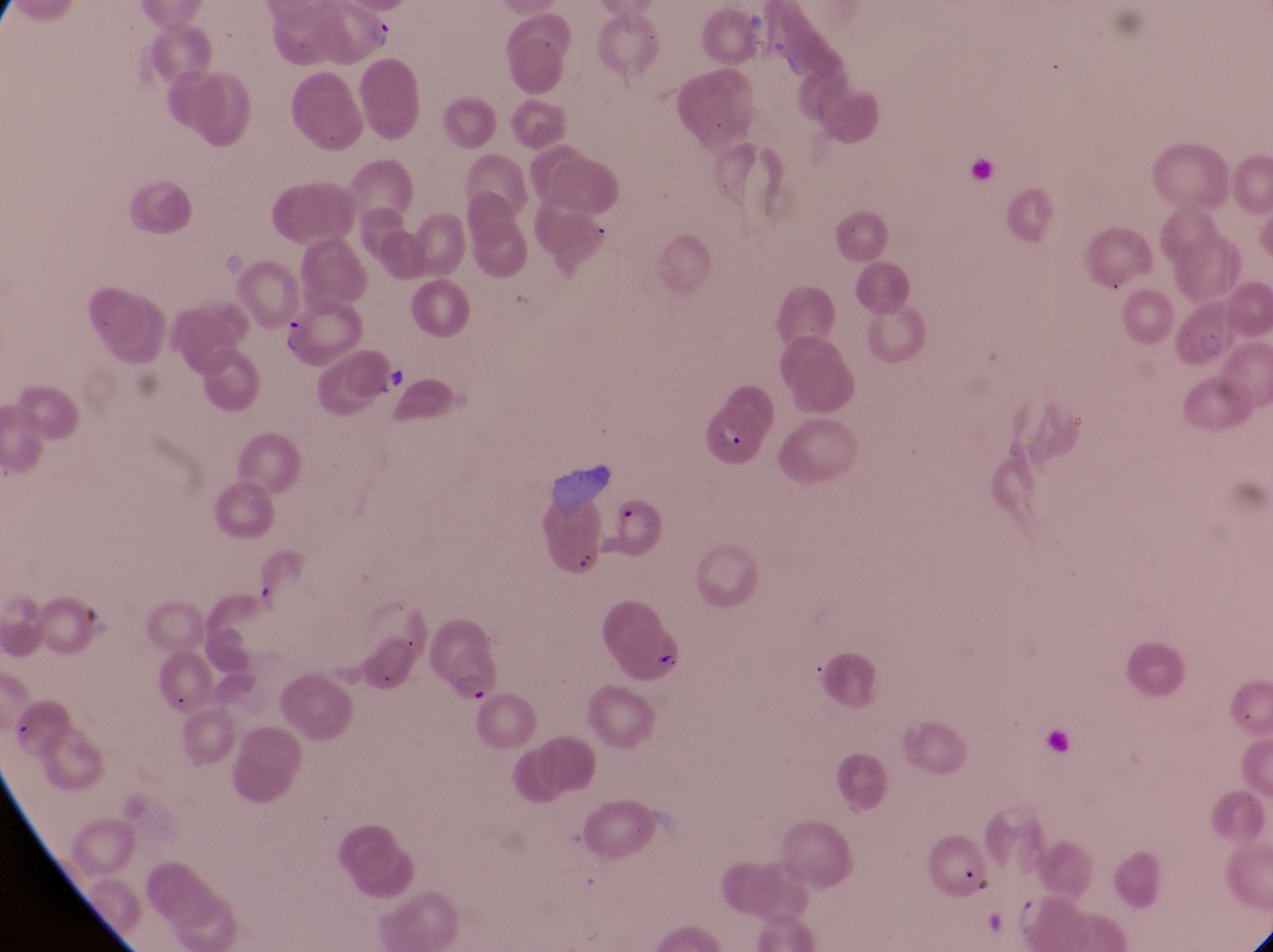 Approximate bounding boxes as left top right bottom in pixels. Parasitised red blood cell locations: 310 5 395 63; 277 307 367 364; 1173 307 1242 372; 698 402 773 468; 608 493 668 554; 539 495 606 580; 594 597 694 689; 422 621 507 708. Image is 1273×952 pixels. Single field of view. Captured by a smartphone held over the eyepiece of an Olympus CX-23 microscope. Sample from Uganda. At a magnification of 1000x. Thin blood smear.